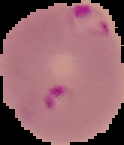

From a thin blood smear. Cell region segmented out of the field of view; the surrounding area is masked to black. Malaria status: parasitized. Image is 124×145 pixels.